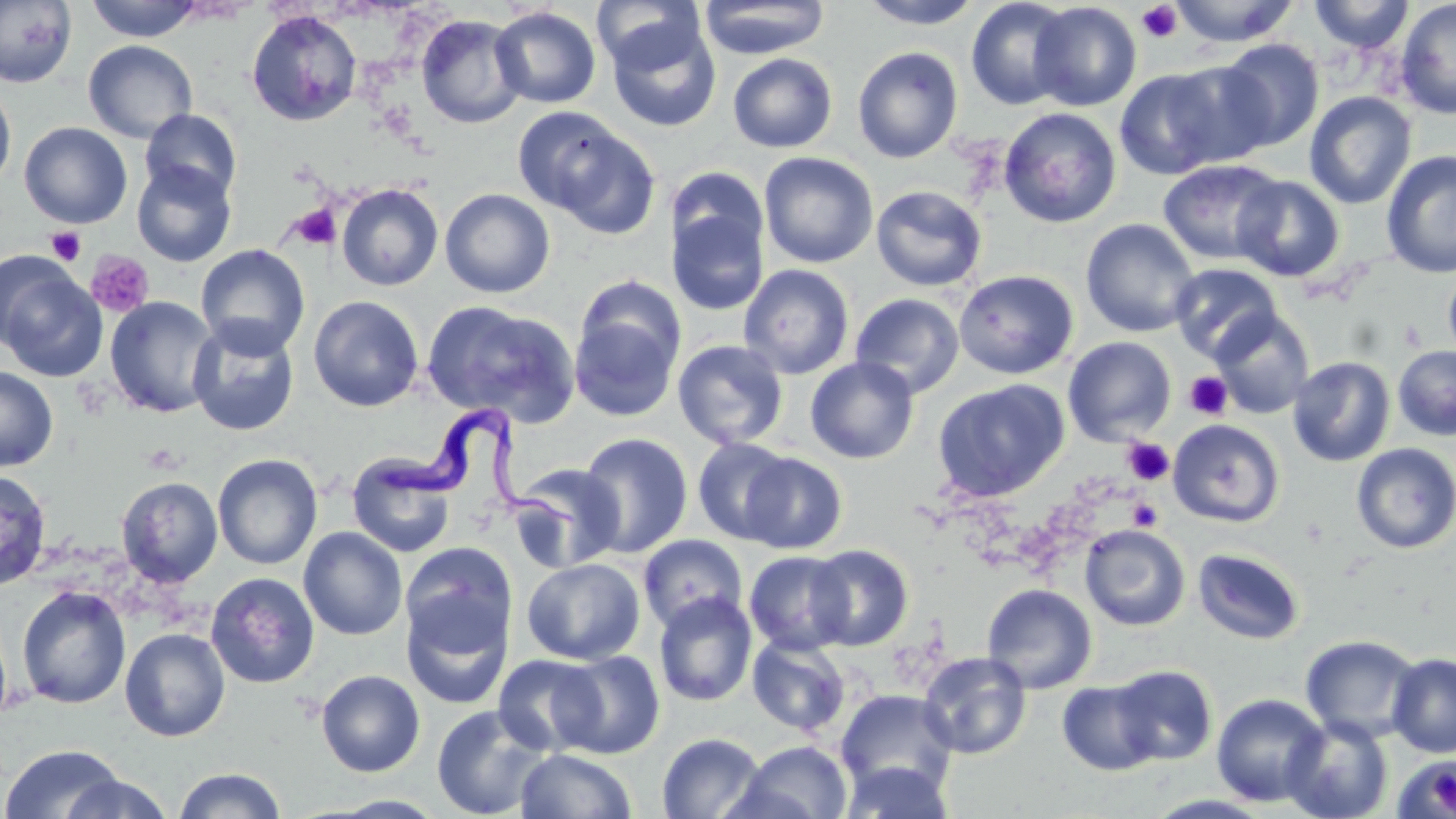

slide_level_diagnosis: Trypanosoma brucei
modality: light microscopy
stain: May-Grünwald-Giemsa
platelet_locations: 'approximate bounding boxes as (x1, y1, x2, y2) in pixels: (1137, 2, 1182, 43), (289, 203, 342, 250), (46, 226, 86, 265), (85, 251, 155, 318), (1184, 371, 1232, 420), (1122, 438, 1174, 486), (141, 443, 184, 475), (1127, 498, 1163, 531)'
image_size: 1456×819 pixels
preparation: thin blood smear
field_of_view: one of a larger specimen
uninfected_red_blood_cell_locations: 'approximate bounding boxes as (x1, y1, x2, y2) in pixels: (84, 0, 205, 42), (859, 0, 983, 29), (965, 0, 1075, 111), (1168, 0, 1299, 46), (1309, 0, 1415, 53), (1394, 0, 1456, 120), (0, 1, 77, 88), (591, 1, 706, 73), (699, 1, 829, 59), (1029, 2, 1142, 111), (490, 6, 601, 109), (246, 10, 363, 127), (415, 14, 528, 129), (605, 19, 722, 133), (1217, 38, 1325, 151), (83, 40, 198, 143), (852, 47, 963, 163), (727, 53, 968, 159), (727, 53, 837, 153), (1160, 59, 1278, 169), (1114, 68, 1231, 180), (0, 81, 16, 194), (1304, 91, 1417, 209), (512, 107, 641, 224), (998, 107, 1122, 228), (139, 109, 242, 203), (19, 122, 133, 229), (1381, 150, 1456, 278), (758, 152, 879, 268), (1157, 159, 1287, 266), (131, 160, 237, 267), (667, 167, 770, 264), (1231, 175, 1345, 282), (336, 183, 444, 291), (870, 185, 987, 292), (440, 188, 555, 298), (667, 205, 769, 315), (1080, 218, 1200, 338), (196, 244, 310, 359), (1, 262, 106, 382), (1169, 263, 1283, 364), (738, 264, 855, 379), (1443, 264, 1456, 365), (954, 269, 1079, 379), (850, 293, 965, 399), (308, 295, 424, 412), (103, 296, 220, 418), (421, 300, 579, 426), (569, 304, 684, 423), (1209, 309, 1315, 419), (186, 318, 300, 436), (1063, 336, 1177, 445), (672, 339, 789, 450), (1392, 345, 1456, 441), (1287, 356, 1396, 467), (805, 357, 919, 464), (0, 366, 58, 471), (932, 379, 1070, 503), (1168, 419, 1285, 528), (577, 433, 694, 557), (692, 437, 795, 545), (1351, 443, 1456, 554), (738, 452, 848, 554), (212, 453, 323, 570), (346, 455, 457, 559), (509, 463, 626, 572), (0, 468, 52, 590), (116, 476, 223, 588), (1079, 524, 1190, 631), (298, 527, 407, 640), (637, 534, 748, 634), (400, 542, 516, 653), (806, 544, 914, 650), (1192, 547, 1305, 645), (744, 550, 855, 656), (522, 557, 645, 665), (205, 571, 320, 689), (981, 583, 1098, 693), (17, 585, 132, 709), (653, 592, 758, 707), (402, 594, 511, 708), (120, 627, 230, 741), (1301, 634, 1421, 744), (747, 636, 851, 736), (552, 650, 665, 759), (917, 651, 1032, 760), (1387, 652, 1456, 758), (492, 654, 604, 756), (1108, 664, 1218, 766), (316, 670, 425, 777), (1057, 679, 1164, 776), (836, 688, 958, 799), (1211, 693, 1330, 807), (431, 704, 554, 819), (1281, 715, 1393, 819), (656, 732, 766, 819), (735, 740, 853, 819), (0, 743, 126, 819), (515, 749, 638, 819), (1393, 753, 1456, 817), (840, 760, 954, 819), (173, 767, 287, 819), (56, 773, 175, 818), (1144, 793, 1277, 818), (318, 794, 451, 817)'
magnification: 1000x
trypanosoma_brucei_locations: 'approximate bounding boxes as (x1, y1, x2, y2) in pixels: (373, 400, 583, 537)'